Locate every Plasmodium ovale-infected red blood cell.
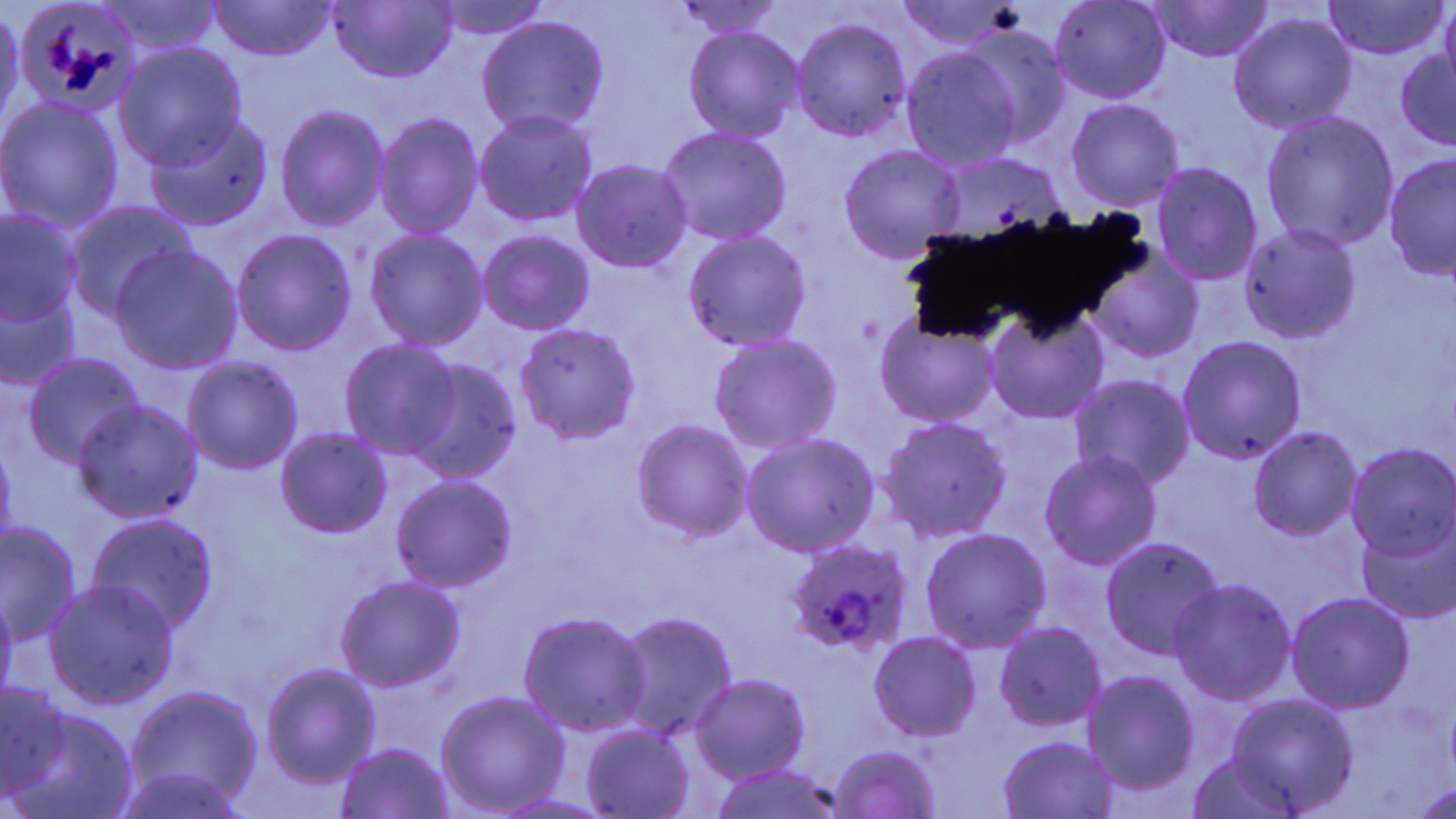
Approximate bounding boxes as (x1, y1, x2, y2) in pixels.
Plasmodium ovale-infected red blood cells: (15, 0, 144, 120), (786, 539, 915, 663).

Uninfected red blood cell locations: (91, 0, 227, 57), (426, 0, 554, 41), (1050, 0, 1169, 103), (327, 1, 460, 84), (670, 1, 787, 38), (893, 1, 1024, 50), (1147, 1, 1275, 63), (1323, 1, 1447, 61), (209, 2, 337, 62), (1439, 2, 1456, 92), (0, 5, 24, 133), (1229, 14, 1355, 133), (477, 15, 610, 138), (790, 17, 913, 143), (683, 25, 803, 142), (963, 26, 1072, 147), (116, 43, 245, 170), (901, 48, 1022, 171), (1395, 48, 1456, 151), (0, 97, 123, 232), (1065, 98, 1185, 212), (275, 105, 389, 231), (475, 110, 598, 226), (375, 112, 484, 239), (1260, 112, 1400, 253), (143, 114, 272, 232), (657, 127, 792, 246), (838, 144, 966, 263), (1384, 155, 1456, 282), (573, 159, 692, 273), (1150, 162, 1263, 287), (66, 203, 196, 324), (0, 212, 82, 327), (1240, 223, 1361, 343), (232, 229, 357, 357), (365, 229, 488, 350), (683, 230, 812, 351), (479, 231, 594, 335), (111, 247, 242, 372), (1087, 248, 1205, 365), (0, 291, 80, 390), (985, 308, 1108, 426), (876, 313, 1000, 428), (513, 323, 640, 443), (708, 334, 842, 455), (1178, 335, 1306, 466), (340, 339, 462, 460), (21, 353, 146, 467), (183, 357, 304, 474), (403, 358, 522, 482), (1070, 374, 1193, 492), (72, 399, 203, 522), (878, 416, 1011, 542), (632, 419, 755, 543), (1249, 426, 1361, 540), (276, 428, 392, 538), (741, 432, 880, 557), (0, 439, 18, 551), (1346, 442, 1456, 563), (1039, 452, 1160, 572), (391, 475, 518, 592), (1355, 511, 1456, 626), (85, 514, 218, 634), (1, 523, 80, 645), (920, 527, 1051, 653), (1101, 538, 1225, 659), (336, 577, 465, 691), (1170, 579, 1296, 704), (46, 580, 179, 709), (0, 591, 16, 706), (1288, 592, 1414, 715), (520, 611, 652, 736), (615, 611, 737, 742), (995, 623, 1107, 731), (869, 632, 980, 740), (261, 665, 379, 789), (1083, 672, 1199, 796), (691, 674, 810, 783), (0, 683, 73, 798), (125, 685, 263, 809), (436, 691, 570, 815), (1229, 694, 1358, 815), (10, 709, 139, 819), (582, 726, 695, 817), (998, 736, 1118, 819), (336, 743, 455, 818), (829, 744, 943, 819), (1184, 758, 1306, 816), (709, 764, 845, 819), (104, 770, 253, 818), (1417, 782, 1456, 819), (495, 794, 611, 817). Slide-level diagnosis: Plasmodium ovale. Single field of view. Captured at 1000x magnification. Thin blood smear. Light microscopy. May-Grünwald-Giemsa stain. Image is 1456×819 pixels.